Evaluate for parasitized red blood cells.
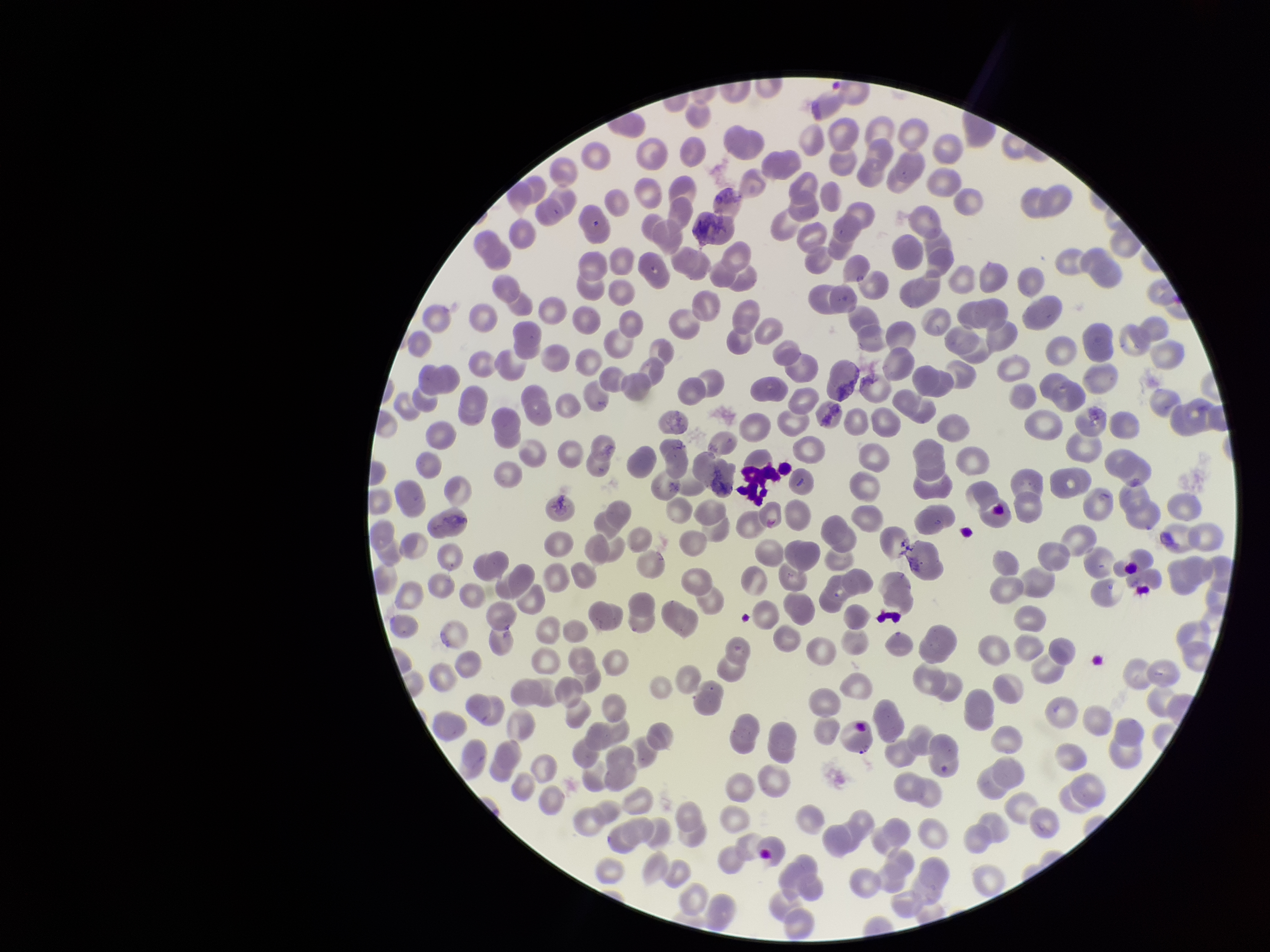

None identified.

patient malaria status = negative
red blood cell count = 267
image size = 1270×952 pixels
parasitized red blood cell count = 0
stain = Giemsa
capture = smartphone photograph through the microscope eyepiece
preparation = thin blood smear
field of view = one from this slide